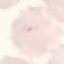

Summary:
  - Malaria status: parasitized
  - Capture: smartphone camera at the microscope eyepiece
  - Stain: Giemsa
  - Preparation: thin blood film
  - Image type: automatically extracted cell patch, resized to 64 × 64 pixels